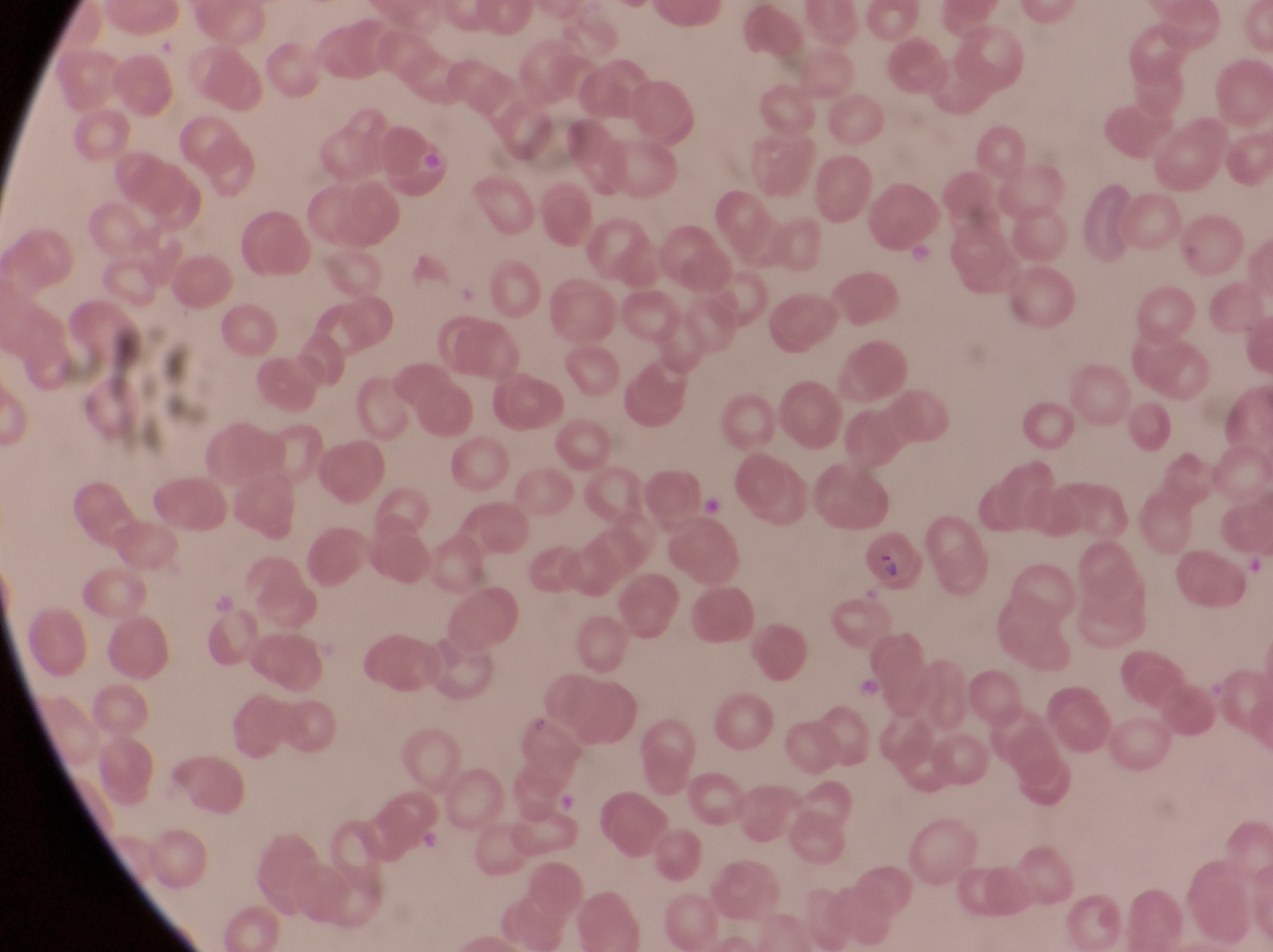

Approximate bounding boxes as (left, top, right, bottom) in pixels.
Summary:
  - Parasitised red blood cell locations: (852, 527, 921, 599), (511, 717, 584, 788)
  - Image size: 1273×952 pixels
  - Field of view: single
  - Country: Uganda
  - Capture: smartphone photograph through the eyepiece of an Olympus CX-23 microscope
  - Preparation: thin blood smear
  - Magnification: 1000x